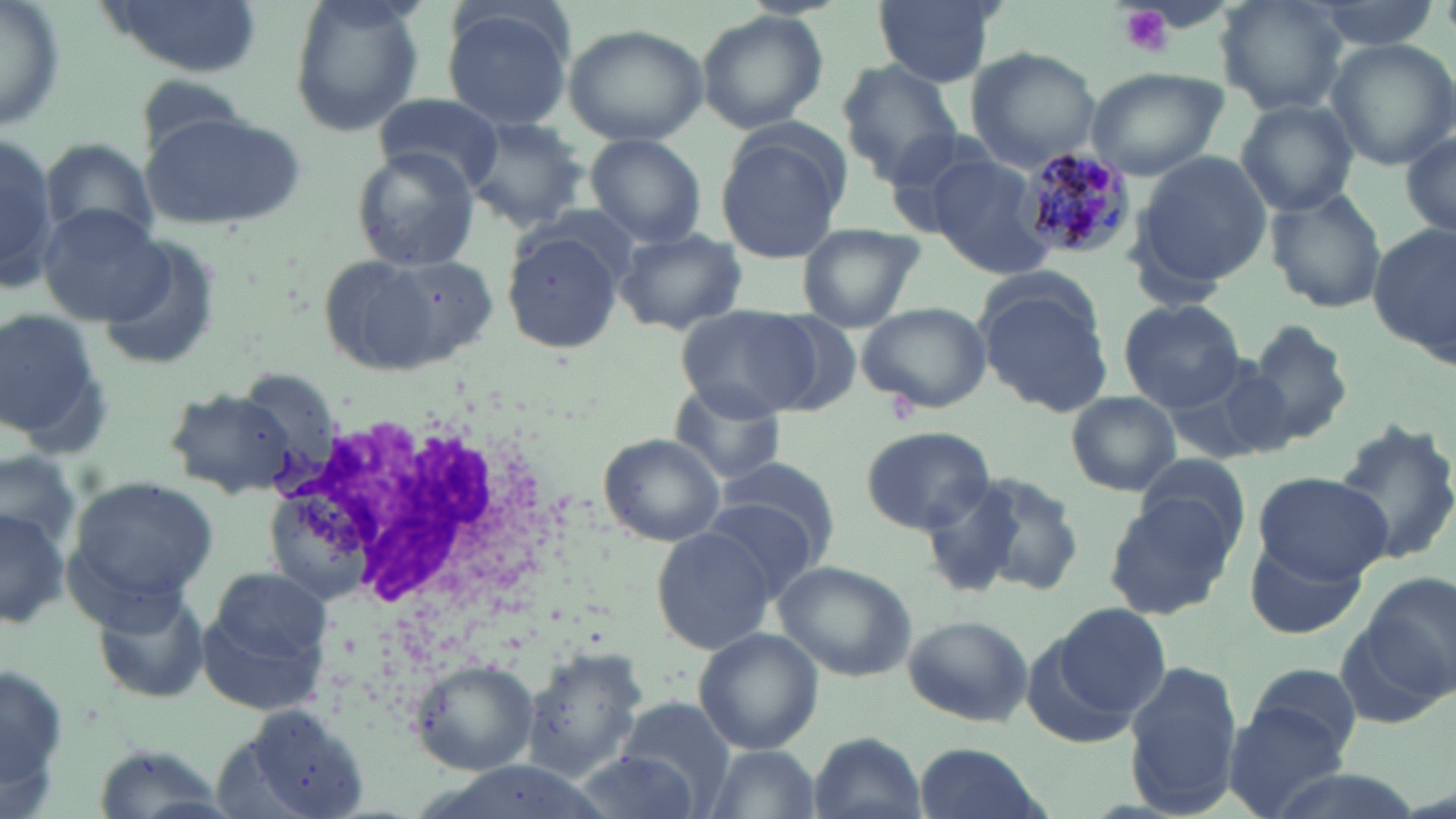

slide_level_diagnosis: Plasmodium malariae
image_size: 1456×819 pixels
uninfected_red_blood_cell_locations: 'approximate bounding boxes as (x1, y1, x2, y2) in pixels: (0, 0, 65, 133), (286, 0, 422, 135), (871, 0, 1002, 87), (1216, 0, 1349, 115), (1297, 0, 1440, 50), (96, 1, 264, 76), (440, 6, 575, 132), (695, 9, 829, 133), (561, 23, 709, 146), (1325, 39, 1456, 170), (964, 46, 1104, 172), (839, 62, 963, 182), (1085, 66, 1227, 181), (374, 93, 505, 192), (1236, 100, 1360, 215), (140, 113, 305, 234), (463, 116, 591, 228), (713, 123, 848, 263), (0, 126, 54, 289), (1400, 131, 1455, 240), (586, 136, 706, 247), (42, 140, 157, 250), (351, 147, 480, 271), (1133, 151, 1274, 287), (926, 154, 1056, 280), (1265, 188, 1387, 315), (35, 205, 166, 325), (796, 223, 923, 332), (1371, 226, 1454, 357), (614, 227, 747, 334), (502, 230, 626, 353), (94, 240, 220, 373), (363, 253, 500, 368), (979, 264, 1101, 353), (978, 284, 1116, 416), (1119, 299, 1245, 411), (857, 301, 991, 415), (677, 304, 820, 419), (0, 306, 103, 442), (751, 309, 866, 417), (1241, 320, 1354, 448), (1164, 357, 1288, 471), (663, 375, 788, 488), (164, 387, 299, 499), (1066, 391, 1181, 496), (1331, 416, 1456, 567), (860, 426, 996, 535), (596, 433, 726, 547), (0, 449, 82, 548), (1134, 451, 1248, 556), (711, 454, 842, 579), (959, 470, 1087, 598), (1252, 473, 1392, 581), (65, 474, 221, 614), (921, 478, 1028, 599), (1102, 495, 1238, 619), (700, 500, 821, 603), (0, 505, 67, 632), (649, 526, 780, 653), (1247, 536, 1366, 640), (772, 557, 919, 683), (198, 571, 332, 712), (1365, 572, 1455, 698), (91, 584, 212, 705), (1051, 602, 1171, 724), (900, 614, 1033, 727), (693, 627, 824, 754), (1021, 631, 1147, 753), (520, 647, 649, 783), (1124, 657, 1242, 815), (410, 659, 537, 775), (1241, 660, 1363, 770), (617, 698, 735, 813), (1225, 702, 1353, 819), (223, 703, 373, 819), (807, 731, 927, 819), (910, 741, 1054, 819), (699, 743, 823, 819), (90, 744, 230, 818), (568, 751, 702, 819)'
plasmodium_malariae_infected_red_blood_cell_locations: 'approximate bounding boxes as (x1, y1, x2, y2) in pixels: (1019, 145, 1139, 262)'
field_of_view: single
stain: May-Grünwald-Giemsa
magnification: 1000x
white_blood_cell_locations: 'approximate bounding boxes as (x1, y1, x2, y2) in pixels: (276, 395, 584, 688)'
platelet_locations: 'approximate bounding boxes as (x1, y1, x2, y2) in pixels: (1118, 4, 1174, 57)'
modality: light microscopy
preparation: thin blood smear